Give the extent of all Plasmodium malariae-infected red blood cells.
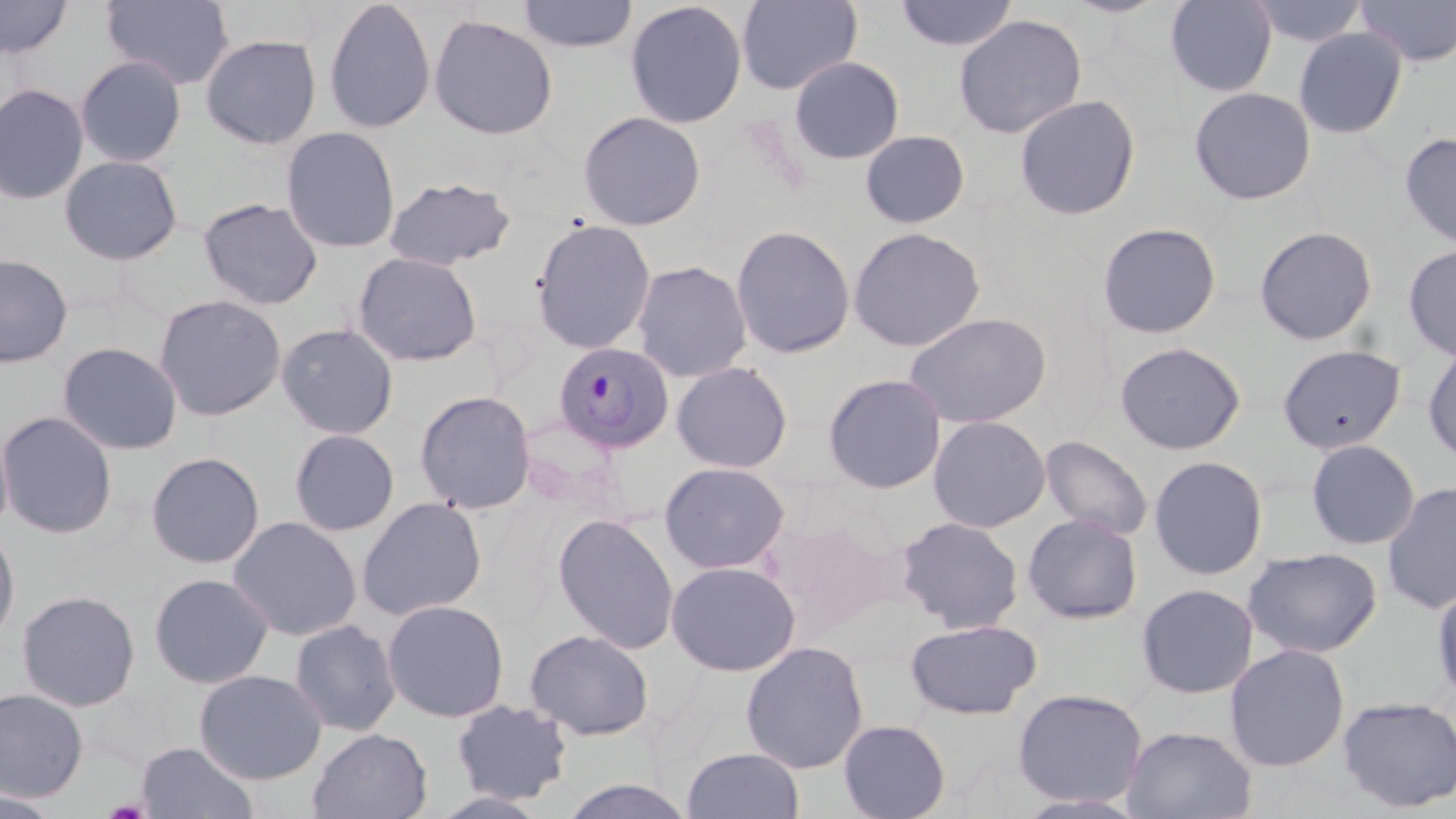

Approximate bounding boxes as (x1, y1, x2, y2) in pixels.
Plasmodium malariae-infected red blood cells: (553, 341, 674, 452).

{
  "slide_level_diagnosis": "Plasmodium malariae",
  "image_size": "1456×819 pixels",
  "uninfected_red_blood_cell_locations": "approximate bounding boxes as (x1, y1, x2, y2) in pixels: (0, 0, 73, 60), (101, 0, 236, 91), (322, 0, 437, 134), (516, 0, 638, 53), (736, 0, 862, 94), (893, 0, 1019, 52), (1164, 0, 1278, 97), (1247, 0, 1370, 49), (1356, 0, 1456, 67), (624, 1, 748, 129), (427, 14, 559, 140), (953, 14, 1087, 139), (1293, 27, 1408, 139), (200, 33, 322, 150), (74, 55, 187, 168), (789, 55, 905, 164), (0, 82, 89, 205), (1189, 86, 1317, 206), (1014, 94, 1141, 221), (577, 110, 707, 231), (280, 126, 401, 253), (859, 129, 971, 229), (1399, 132, 1456, 249), (59, 154, 184, 266), (383, 175, 517, 271), (197, 197, 324, 309), (530, 218, 657, 354), (1096, 222, 1222, 339), (730, 224, 856, 359), (1254, 225, 1378, 345), (848, 227, 986, 351), (1402, 242, 1456, 360), (352, 252, 483, 367), (0, 253, 74, 367), (631, 260, 753, 382), (153, 293, 288, 421), (904, 312, 1052, 429), (276, 322, 400, 440), (1422, 339, 1456, 466), (57, 341, 183, 455), (1114, 341, 1246, 455), (1277, 343, 1407, 454), (671, 361, 794, 473), (822, 372, 947, 494), (414, 390, 538, 514), (0, 410, 118, 540), (928, 415, 1051, 533), (0, 417, 15, 539), (288, 428, 400, 536), (1039, 434, 1154, 541), (1305, 439, 1421, 551), (145, 451, 266, 569), (1148, 455, 1269, 580), (658, 461, 791, 573), (1381, 480, 1456, 615), (356, 496, 488, 621), (1021, 512, 1143, 625), (552, 513, 680, 654), (766, 514, 904, 635), (227, 515, 363, 641), (895, 515, 1025, 633), (0, 524, 21, 650), (1242, 546, 1383, 659), (666, 560, 801, 676), (148, 572, 275, 689), (1430, 580, 1456, 703), (1135, 583, 1259, 699), (16, 589, 141, 711), (381, 598, 510, 723), (289, 618, 402, 736), (905, 618, 1043, 720), (524, 628, 655, 741), (740, 640, 869, 774), (1224, 642, 1350, 771), (193, 668, 327, 784), (0, 687, 89, 802), (1011, 687, 1149, 808), (1337, 695, 1456, 813), (449, 699, 574, 806), (837, 719, 952, 819), (1121, 725, 1258, 819), (308, 728, 432, 819), (136, 740, 259, 819), (681, 746, 806, 819), (556, 778, 700, 818), (0, 788, 66, 818), (1011, 792, 1151, 817)",
  "preparation": "thin blood film",
  "field_of_view": "single",
  "magnification": "1000x",
  "stain": "May-Grünwald-Giemsa",
  "modality": "light microscopy"
}